Report the malaria status of this cell.
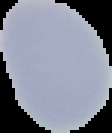

It is uninfected.

Summary:
  - Image type: cell region segmented out of the field of view; surrounding area masked to black
  - Image size: 112×133 pixels
  - Preparation: thin blood film